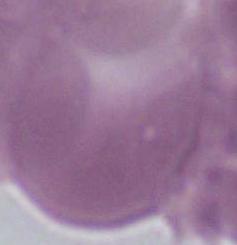 A red blood cell is shown. Captured at 1000x magnification. Micrograph.